State which parasite is depicted.
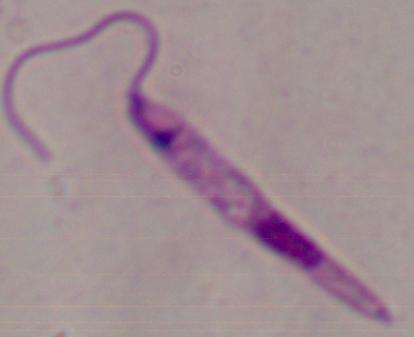

This is Leishmania.

modality = micrograph
magnification = 1000x